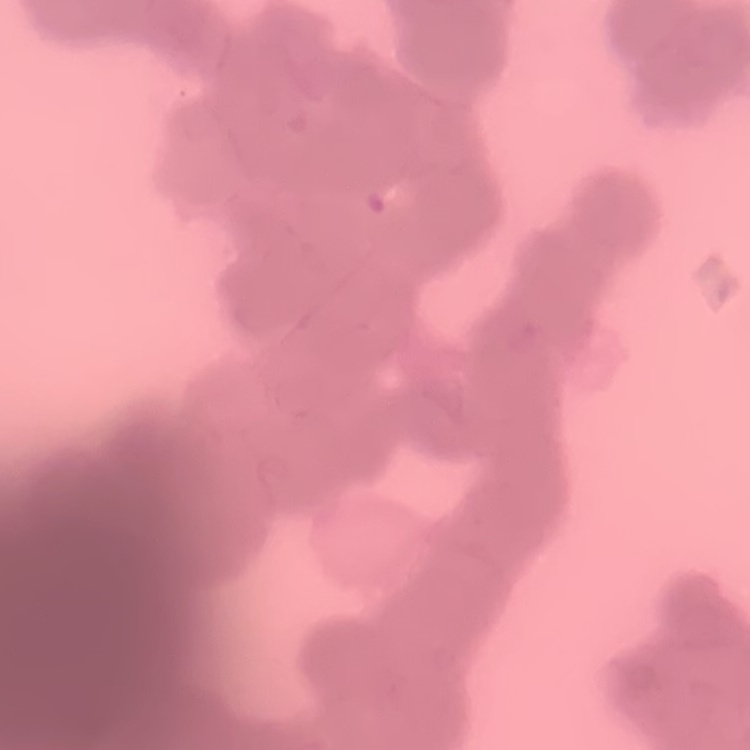
The erythrocytes show rouleaux formation. Stained with either Field's or Giemsa. Thin blood smear. One tile cut from a larger photomicrograph.